Describe the morphology of the red blood cells.
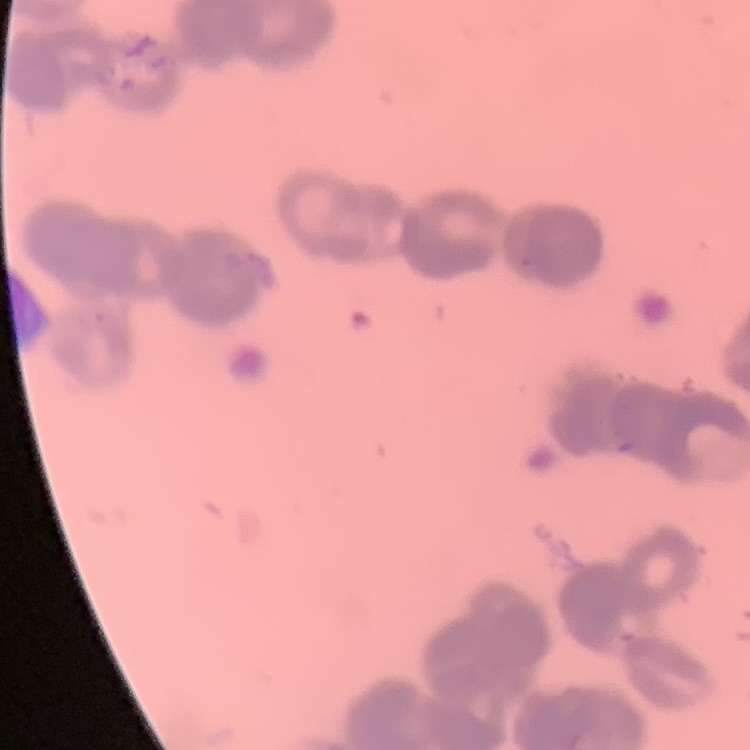
They show rouleaux formation.

Summary:
  - Stain: Field's or Giemsa
  - Image type: square crop of a larger photomicrograph
  - Preparation: thin peripheral smear